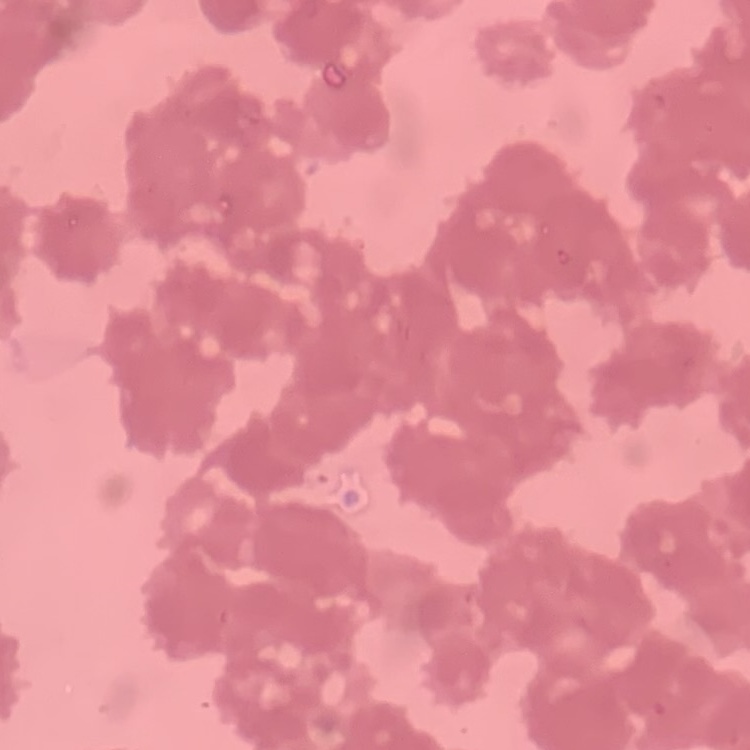
The erythrocytes show rouleaux formation. Field's or Giemsa stain. One tile cut from a larger photomicrograph. Thin peripheral smear.